Name the cell type shown.
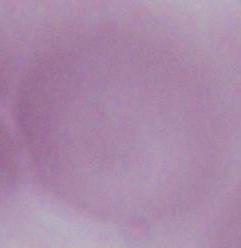
An erythrocyte.

Summary:
  - Magnification: 1000x
  - Modality: photomicrograph